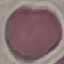
Summary:
  - Result: no malaria parasites detected
  - Image type: cell patch, automatically extracted from a larger field of view and resized to 64 × 64 pixels
  - Stain: Giemsa
  - Preparation: thin smear
  - Capture: smartphone camera at the microscope eyepiece